Locate every leukocyte (white blood cell).
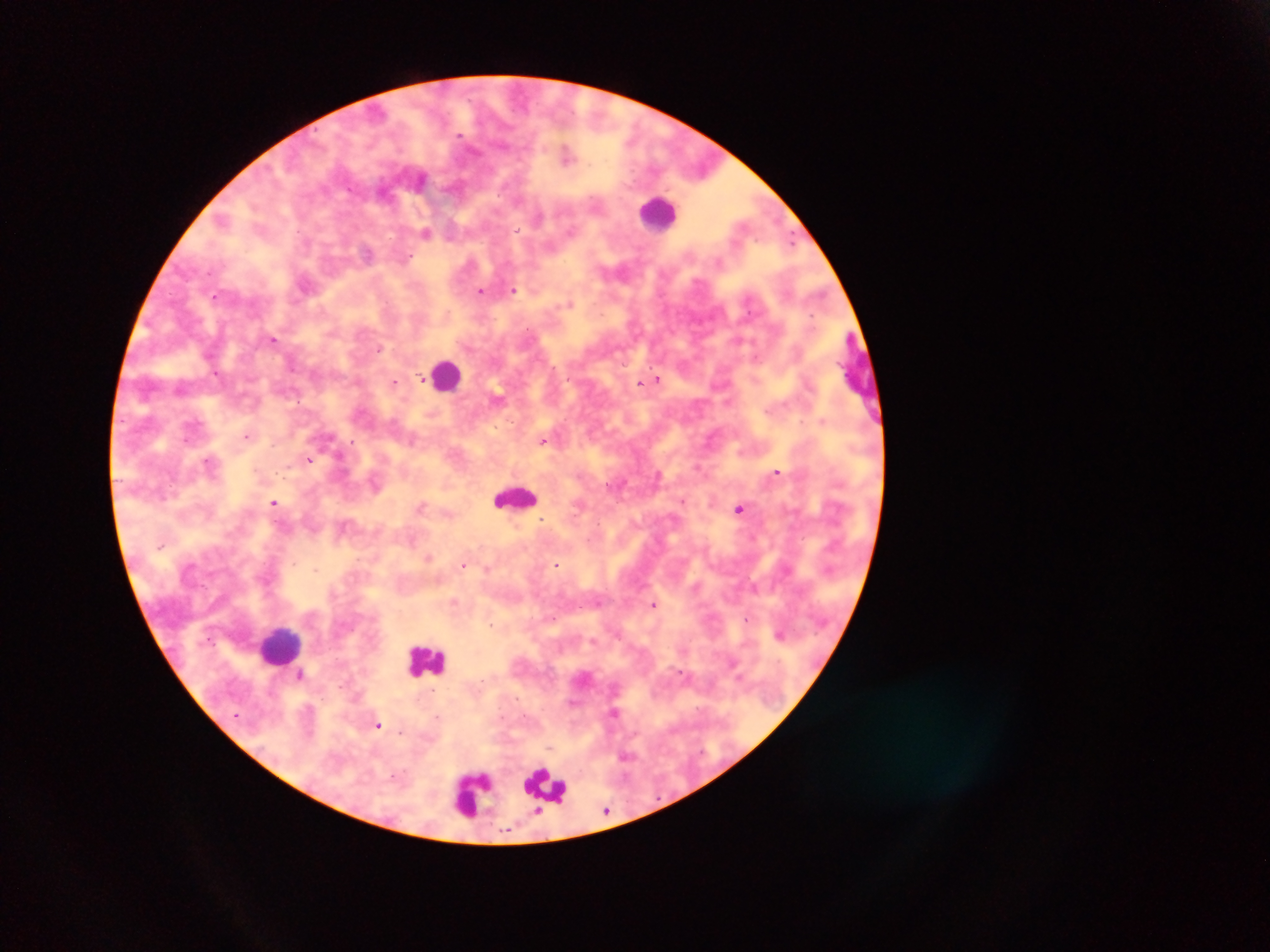
Approximate centers as x y in pixels.
Leukocytes: 658 213; 448 374; 514 497; 280 644; 426 660; 546 787; 471 794.

Summary:
  - Plasmodium parasite locations: 461 135; 567 155; 420 179; 539 216; 572 231; 426 233; 792 241; 367 252; 482 290; 514 290; 214 297; 570 302; 812 317; 274 339; 380 348; 423 380; 658 380; 395 382; 640 383; 247 436; 352 441; 411 442; 542 442; 340 456; 309 459; 208 461; 698 467; 776 472; 658 474; 682 501; 274 502; 421 507; 739 509; 542 519; 412 540; 428 557; 463 565; 556 565; 315 569; 486 569; 453 602; 654 604; 551 618; 490 624; 779 634; 300 675; 614 712; 437 717; 379 725; 607 810
  - Capture: mobile-phone photograph through a microscope
  - Country: Ghana
  - Preparation: thick blood smear
  - Field of view: single
  - Image size: 1270×952 pixels